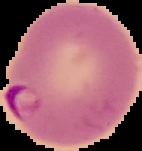
From a thin blood smear. Segmented cell region on a black background. Image is 142×151 pixels. Result: malaria parasites identified.